Give the position of every Plasmodium parasite and every leukocyte.
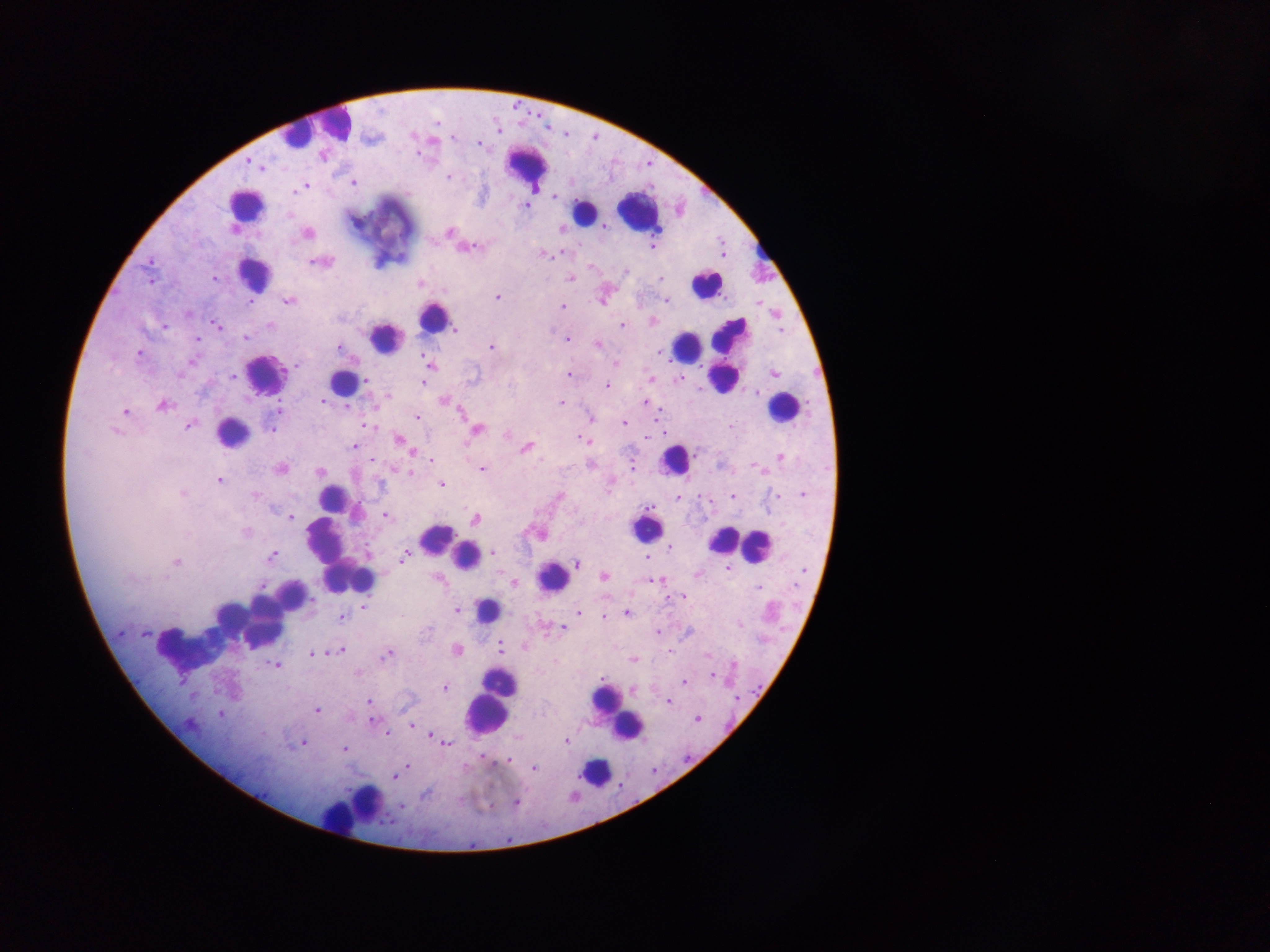
Approximate centers as x y in pixels.
Plasmodium parasites: 479 144; 250 162; 448 177; 354 183; 302 187; 298 189; 526 206; 448 232; 307 233; 653 246; 468 248; 543 254; 318 262; 626 271; 214 278; 571 278; 661 279; 496 297; 666 300; 249 302; 288 302; 562 307; 653 321; 216 325; 164 326; 270 326; 622 326; 455 329; 245 337; 196 338; 567 339; 597 345; 491 347; 339 348; 659 351; 138 353; 193 362; 615 363; 429 365; 297 367; 570 374; 774 374; 233 376; 652 379; 366 381; 423 382; 607 386; 387 396; 322 401; 445 401; 645 401; 561 403; 163 405; 124 412; 589 417; 418 418; 624 423; 189 425; 367 425; 271 428; 476 430; 116 431; 507 434; 400 440; 585 440; 353 446; 525 447; 411 452; 781 457; 372 460; 432 460; 591 464; 752 465; 633 467; 280 468; 481 469; 320 472; 409 473; 219 480; 442 484; 182 493; 803 494; 255 495; 777 495; 559 496; 733 496; 677 497; 290 516; 385 516; 475 519; 245 532; 670 547; 493 553; 271 556; 405 556; 646 556; 177 562; 578 564; 728 569; 697 574; 604 576; 652 580; 514 584; 261 586; 758 588; 675 597; 683 597; 363 607; 456 610; 578 612; 626 613; 603 616; 341 617; 428 629; 562 629; 657 632; 145 634; 501 648; 340 650; 457 650; 669 652; 312 654; 386 655; 707 655; 634 660; 734 664; 274 665; 712 675; 684 681; 445 688; 368 701; 668 702; 317 710; 219 714; 697 719; 372 721; 411 725; 386 735; 433 735; 566 741; 304 743; 445 743; 344 749; 509 760; 408 767; 534 768; 394 776; 425 795; 516 802; 401 806.
Leukocytes (some below the resolvable threshold): 328 125; 295 137; 527 165; 246 206; 637 211; 583 213; 759 251; 254 273; 706 283; 432 317; 731 336; 384 337; 685 347; 265 374; 724 377; 339 386; 782 409; 232 433; 673 460; 332 499; 646 528; 436 538; 741 542; 757 547; 451 549; 719 549; 338 554; 466 556; 553 576; 358 580; 289 599; 487 611; 229 617; 263 625; 184 647; 501 682; 605 704; 487 712; 626 725; 595 772; 355 806.

Thick blood film. One field of view. Mobile-phone photograph taken through the microscope. Image is 1270×952 pixels. Collected in Ghana.